Name the parasite shown.
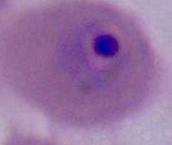
Plasmodium.

Micrograph. 400x or 1000x magnification.